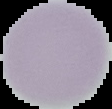

{
  "image_size": "112×109 pixels",
  "result": "no Plasmodium parasites detected",
  "image_type": "cell region segmented out of the field of view; surrounding area masked to black",
  "preparation": "thin blood smear"
}